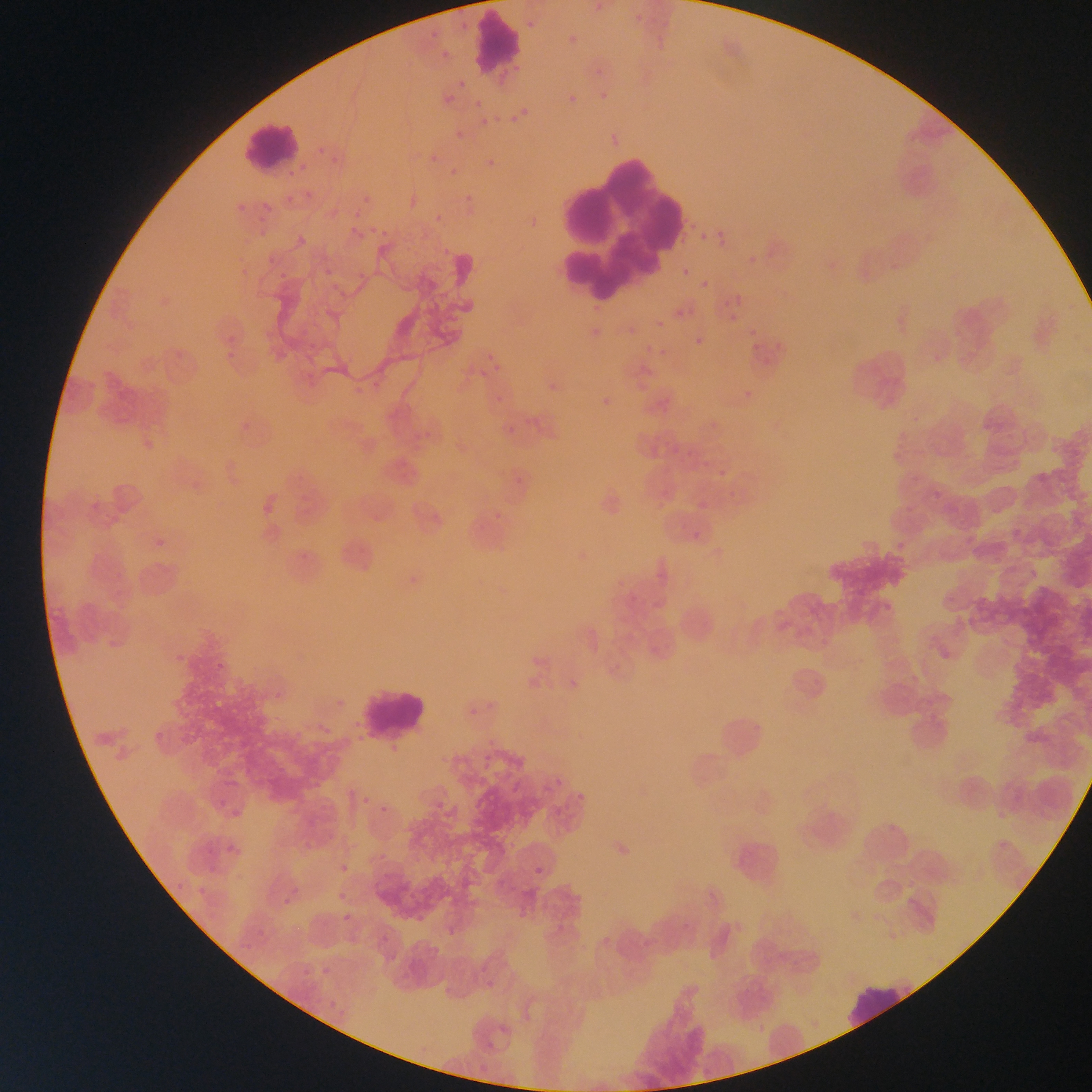
capture = mobile-phone photograph through a microscope
country = Ghana
field of view = single
leukocyte locations = approximate bounding boxes as (left, top, right, bottom) in pixels: (471, 17, 527, 71), (243, 118, 301, 172), (541, 132, 692, 313), (357, 683, 426, 739), (711, 704, 776, 768), (728, 828, 787, 895), (844, 978, 916, 1029)
preparation = thin blood smear
malaria parasite locations = approximate bounding boxes as (left, top, right, bottom) in pixels: (523, 16, 538, 34), (565, 30, 583, 51), (453, 77, 470, 95), (595, 88, 613, 107), (564, 91, 582, 110), (439, 92, 457, 109), (472, 96, 486, 109), (516, 104, 533, 121), (508, 113, 521, 127), (477, 115, 493, 130), (451, 127, 468, 143), (427, 152, 440, 167), (483, 154, 502, 172), (447, 164, 464, 181), (460, 190, 478, 208), (360, 192, 375, 207), (689, 225, 709, 245), (714, 228, 731, 248), (292, 231, 312, 250), (697, 232, 709, 243), (744, 246, 771, 273), (744, 252, 762, 270), (679, 266, 691, 279), (276, 267, 293, 284), (697, 277, 712, 291), (730, 290, 748, 309), (671, 306, 687, 321), (654, 318, 667, 330), (744, 333, 765, 358), (691, 334, 707, 351), (656, 346, 671, 361), (927, 346, 951, 374), (543, 378, 565, 400), (738, 384, 760, 408), (597, 392, 618, 413), (503, 423, 519, 438), (359, 792, 374, 809), (531, 862, 548, 880), (340, 910, 356, 928)
image size = 1092×1092 pixels